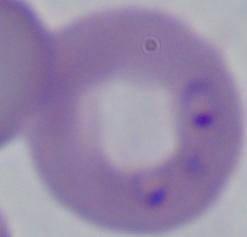
identification: Babesia
magnification: 1000x
modality: micrograph